Name the parasite shown.
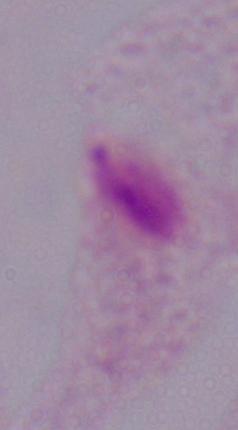
This is a trichomonad.

1000x magnification. Photomicrograph.